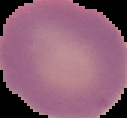 Image is 127×118 pixels. Malaria status: uninfected. From a thin blood smear. Segmented cell region on a black background.